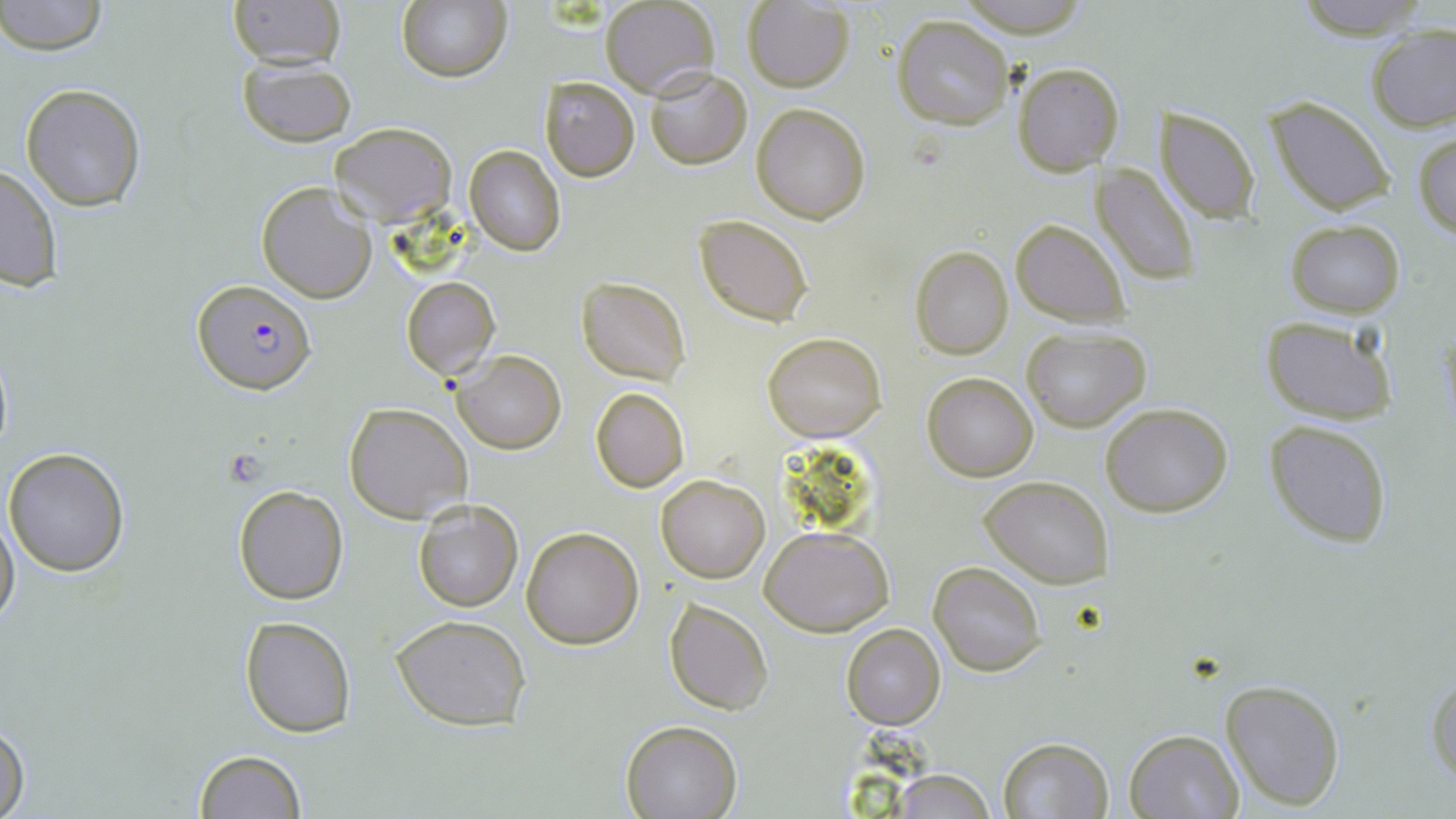

Summary:
  - Coordinate format: approximate bounding boxes as named x1/y1/x2/y2 corners in pixels
  - Uninfected red blood cell locations: (x1=1, y1=0, x2=108, y2=55), (x1=227, y1=0, x2=344, y2=68), (x1=1288, y1=0, x2=1438, y2=37), (x1=601, y1=1, x2=718, y2=99), (x1=958, y1=1, x2=1094, y2=37), (x1=396, y1=2, x2=512, y2=83), (x1=743, y1=2, x2=856, y2=92), (x1=893, y1=16, x2=1012, y2=129), (x1=1364, y1=26, x2=1456, y2=133), (x1=237, y1=56, x2=357, y2=148), (x1=1013, y1=61, x2=1123, y2=175), (x1=645, y1=69, x2=752, y2=168), (x1=538, y1=75, x2=640, y2=182), (x1=20, y1=84, x2=146, y2=210), (x1=1265, y1=96, x2=1394, y2=215), (x1=750, y1=101, x2=871, y2=224), (x1=1155, y1=105, x2=1261, y2=224), (x1=330, y1=124, x2=457, y2=225), (x1=1413, y1=129, x2=1456, y2=238), (x1=463, y1=144, x2=566, y2=256), (x1=0, y1=163, x2=64, y2=291), (x1=1090, y1=164, x2=1202, y2=286), (x1=256, y1=182, x2=378, y2=302), (x1=695, y1=214, x2=813, y2=326), (x1=1010, y1=218, x2=1129, y2=326), (x1=1285, y1=219, x2=1405, y2=318), (x1=910, y1=245, x2=1012, y2=359), (x1=401, y1=275, x2=500, y2=379), (x1=576, y1=277, x2=690, y2=384), (x1=1259, y1=316, x2=1398, y2=425), (x1=1437, y1=316, x2=1456, y2=434), (x1=1020, y1=327, x2=1151, y2=432), (x1=763, y1=331, x2=887, y2=442), (x1=451, y1=350, x2=565, y2=455), (x1=922, y1=372, x2=1038, y2=481), (x1=591, y1=387, x2=689, y2=493), (x1=345, y1=402, x2=473, y2=523), (x1=1100, y1=402, x2=1233, y2=518), (x1=1264, y1=419, x2=1392, y2=546), (x1=4, y1=447, x2=130, y2=577), (x1=656, y1=474, x2=770, y2=583), (x1=980, y1=475, x2=1112, y2=587), (x1=234, y1=485, x2=349, y2=604), (x1=411, y1=499, x2=525, y2=613), (x1=1, y1=508, x2=18, y2=634), (x1=761, y1=526, x2=894, y2=636), (x1=520, y1=527, x2=644, y2=649), (x1=929, y1=561, x2=1045, y2=676), (x1=664, y1=598, x2=773, y2=715), (x1=239, y1=614, x2=357, y2=738), (x1=390, y1=614, x2=534, y2=731), (x1=841, y1=623, x2=946, y2=730), (x1=1427, y1=669, x2=1456, y2=790), (x1=1219, y1=678, x2=1346, y2=811), (x1=0, y1=716, x2=30, y2=819), (x1=621, y1=718, x2=742, y2=819), (x1=1124, y1=728, x2=1243, y2=818), (x1=995, y1=736, x2=1115, y2=819), (x1=194, y1=749, x2=306, y2=819), (x1=887, y1=767, x2=996, y2=819)
  - Plasmodium falciparum-infected red blood cell locations: (x1=192, y1=279, x2=317, y2=394)
  - Slide-level diagnosis: Plasmodium falciparum
  - Preparation: thin blood smear
  - Modality: optical microscopy
  - Field of view: single
  - Stain: May-Grünwald-Giemsa
  - Magnification: 1000x
  - Image size: 1456×819 pixels